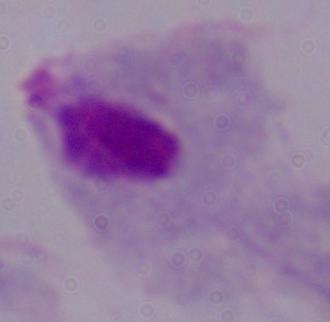

magnification = 1000x
modality = photomicrograph
identification = trichomonad